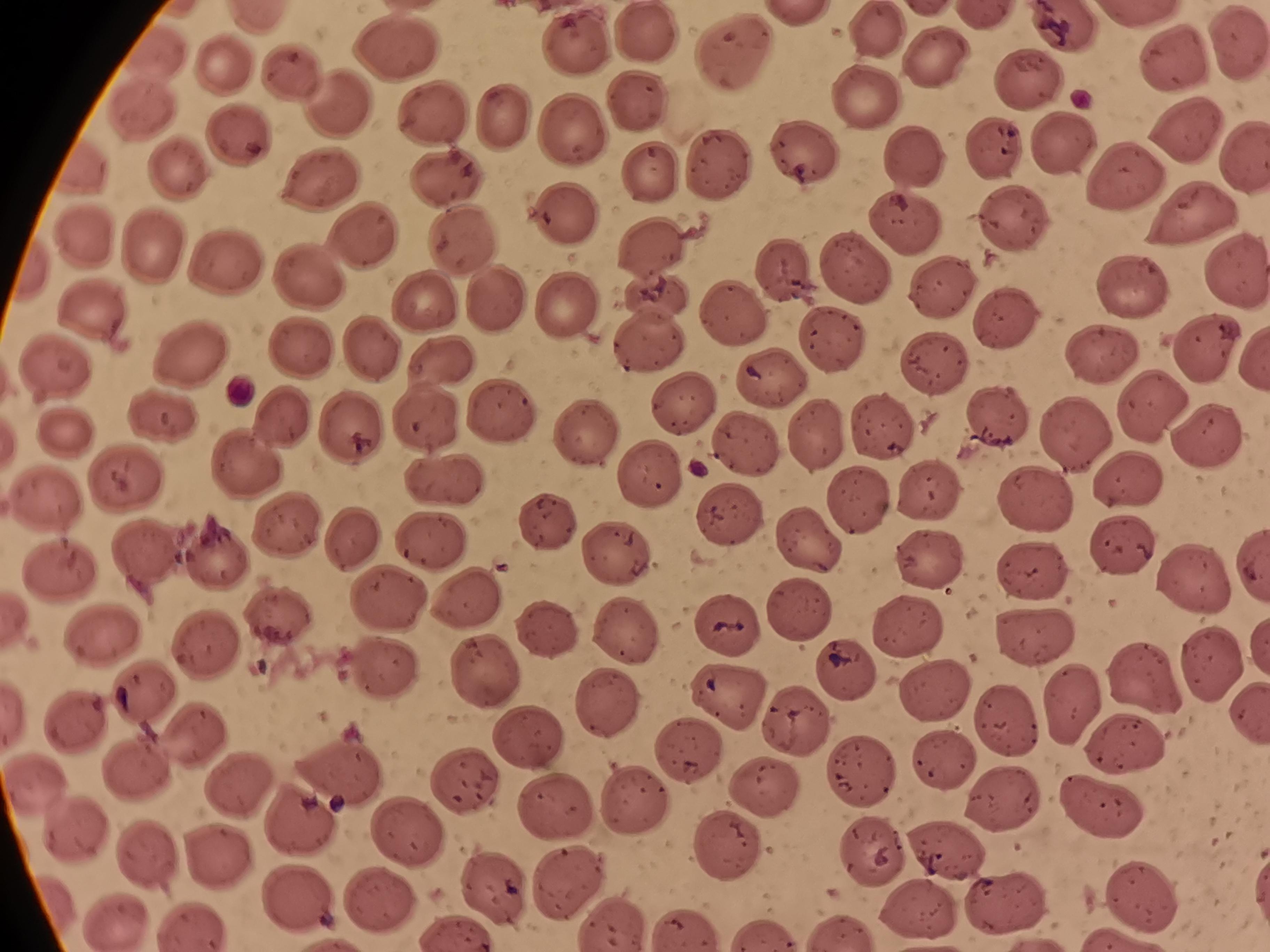 Approximate centers as (x, y) in pixels. Cell locations: (647, 31), (878, 31), (1239, 44), (574, 48), (399, 50), (739, 50), (933, 55), (1178, 56), (228, 65), (297, 73), (1033, 76), (869, 92), (340, 97), (637, 104), (146, 115), (435, 116), (505, 119), (1182, 123), (572, 132), (234, 138), (1061, 139), (998, 147), (1246, 154), (808, 155), (911, 156), (723, 164), (183, 168), (656, 174), (1123, 177), (323, 180), (447, 181), (562, 209), (1198, 213), (1012, 218), (908, 219), (361, 235), (89, 238), (150, 247), (456, 248), (1237, 263), (858, 265), (226, 266), (300, 271), (788, 273), (1133, 282), (942, 289), (646, 290), (486, 298), (426, 305), (560, 310), (98, 311), (737, 317), (1004, 321), (828, 338), (301, 348), (1212, 348), (372, 354), (1103, 355), (189, 359), (438, 365), (936, 365), (53, 368), (775, 379), (685, 398), (1152, 400), (501, 413), (164, 415), (427, 417), (1002, 418), (282, 422), (587, 428), (351, 430), (880, 431), (1212, 434), (69, 435), (745, 444), (242, 460), (652, 477), (125, 480), (1136, 480), (439, 483), (932, 493), (46, 498), (855, 499), (1042, 499), (731, 517), (543, 523), (287, 527), (353, 539), (432, 539), (806, 542), (1120, 548), (622, 550), (145, 551), (218, 552), (925, 558), (1036, 568), (64, 575), (1193, 576), (471, 594), (391, 596), (800, 609), (281, 615), (907, 625), (724, 627), (626, 630), (108, 631), (550, 631), (1039, 641), (210, 643), (382, 666), (842, 669), (1208, 671), (486, 672), (1142, 676), (938, 690), (736, 695), (152, 697), (1071, 706), (608, 710), (1010, 716), (77, 724), (793, 728), (529, 732), (1133, 739), (199, 741), (696, 746), (950, 763), (341, 769), (860, 775), (130, 776), (471, 782), (243, 786), (763, 786), (637, 800), (1004, 802), (1104, 803), (562, 807), (302, 820), (71, 830), (413, 831), (725, 848), (948, 848), (153, 854), (878, 854), (217, 856), (568, 879), (494, 889), (301, 893), (1011, 899), (1144, 901), (381, 906), (924, 912), (613, 921), (116, 922), (196, 926), (686, 930), (767, 934). Photographed with a smartphone camera at the microscope eyepiece. Image is 1270×952 pixels. Thin blood smear. Single field of view. Giemsa stain.